Identify the blood parasite species.
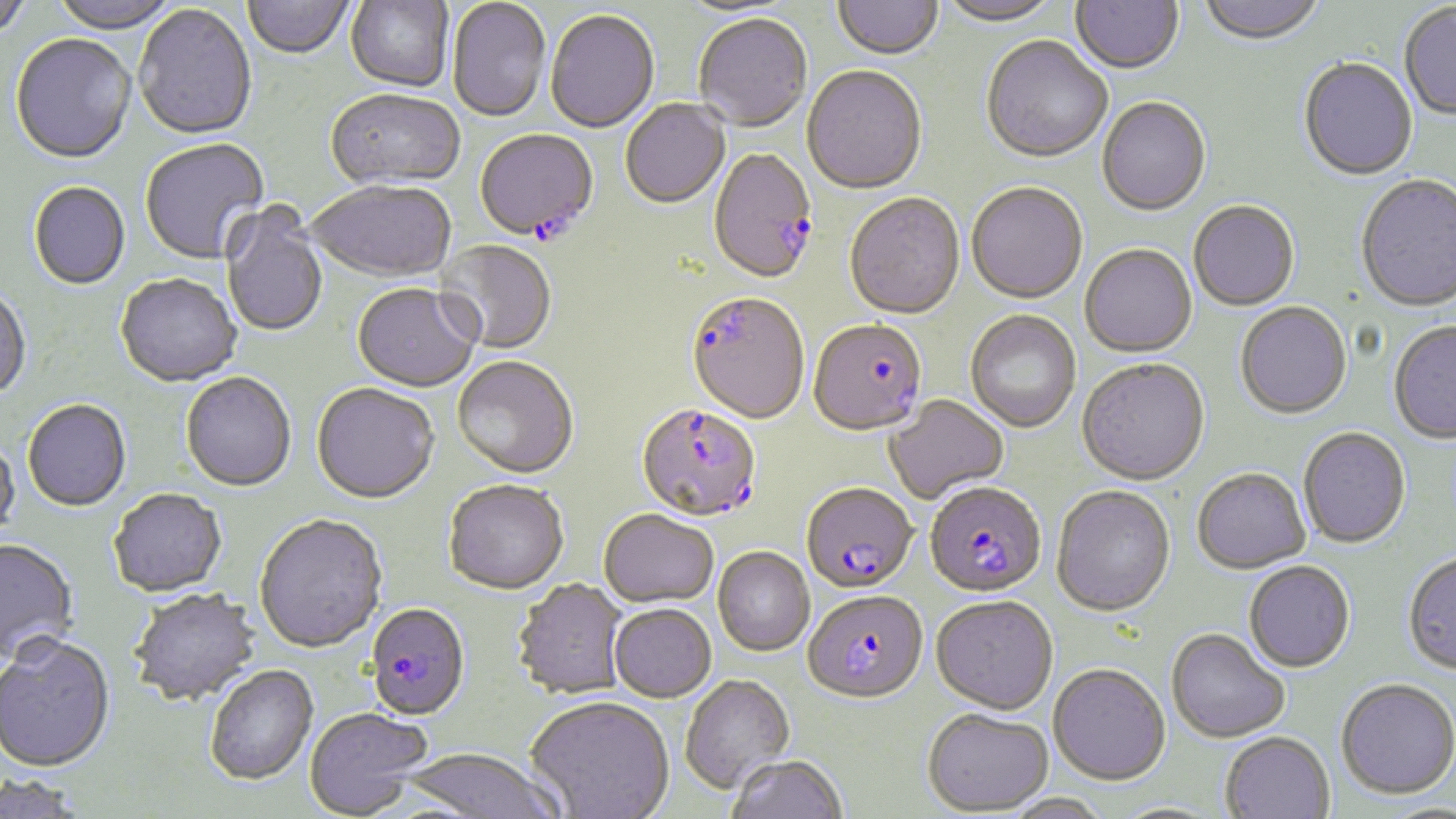
Plasmodium falciparum.

{
  "modality": "light microscopy",
  "magnification": "1000x",
  "plasmodium_falciparum_infected_red_blood_cell_locations": "approximate bounding boxes as (x1, y1, x2, y2) in pixels: (474, 130, 598, 244), (709, 150, 818, 286), (686, 294, 809, 426), (809, 321, 927, 439), (636, 404, 762, 524), (801, 484, 918, 594), (924, 484, 1046, 599), (803, 591, 928, 705), (365, 603, 470, 721)",
  "uninfected_red_blood_cell_locations": "approximate bounding boxes as (x1, y1, x2, y2) in pixels: (0, 0, 34, 42), (47, 0, 182, 35), (833, 0, 942, 62), (936, 0, 1063, 28), (1071, 0, 1184, 77), (1197, 0, 1326, 49), (243, 1, 354, 61), (345, 1, 454, 94), (446, 1, 551, 124), (1399, 4, 1456, 123), (133, 5, 257, 142), (546, 11, 659, 135), (694, 16, 813, 134), (10, 35, 137, 167), (981, 38, 1112, 165), (1298, 59, 1418, 183), (801, 67, 927, 197), (325, 90, 465, 193), (1097, 98, 1211, 218), (621, 100, 731, 210), (140, 139, 270, 266), (1356, 176, 1456, 314), (28, 183, 131, 291), (308, 183, 456, 285), (966, 184, 1088, 306), (844, 194, 965, 321), (1189, 202, 1300, 312), (220, 203, 328, 339), (433, 240, 556, 355), (1080, 245, 1197, 359), (115, 275, 241, 389), (351, 285, 480, 394), (0, 288, 31, 402), (1235, 303, 1352, 421), (965, 311, 1081, 433), (1388, 322, 1456, 445), (452, 358, 579, 480), (1076, 361, 1210, 487), (180, 374, 296, 493), (311, 384, 440, 506), (884, 395, 1009, 505), (22, 401, 132, 513), (1298, 428, 1411, 549), (0, 436, 20, 542), (1192, 470, 1311, 575), (442, 481, 569, 596), (1051, 487, 1176, 619), (109, 491, 227, 600), (599, 510, 719, 608), (254, 515, 388, 655), (0, 539, 79, 668), (713, 548, 815, 657), (1403, 554, 1456, 677), (1244, 562, 1356, 674), (513, 580, 628, 700), (128, 590, 263, 709), (932, 597, 1059, 716), (609, 605, 716, 703), (1166, 630, 1290, 745), (0, 639, 116, 775), (1048, 665, 1171, 787), (204, 666, 318, 787), (679, 676, 796, 795), (1336, 680, 1456, 800), (524, 697, 674, 818), (304, 707, 432, 818), (922, 708, 1054, 816), (1220, 733, 1335, 819), (398, 749, 570, 819), (727, 755, 848, 819), (0, 775, 89, 818), (1003, 793, 1112, 819), (1107, 801, 1230, 819)",
  "preparation": "thin blood smear",
  "image_size": "1456×819 pixels",
  "field_of_view": "single",
  "stain": "May-Grünwald-Giemsa"
}